Give the extent of all Plasmodium falciparum-infected red blood cells.
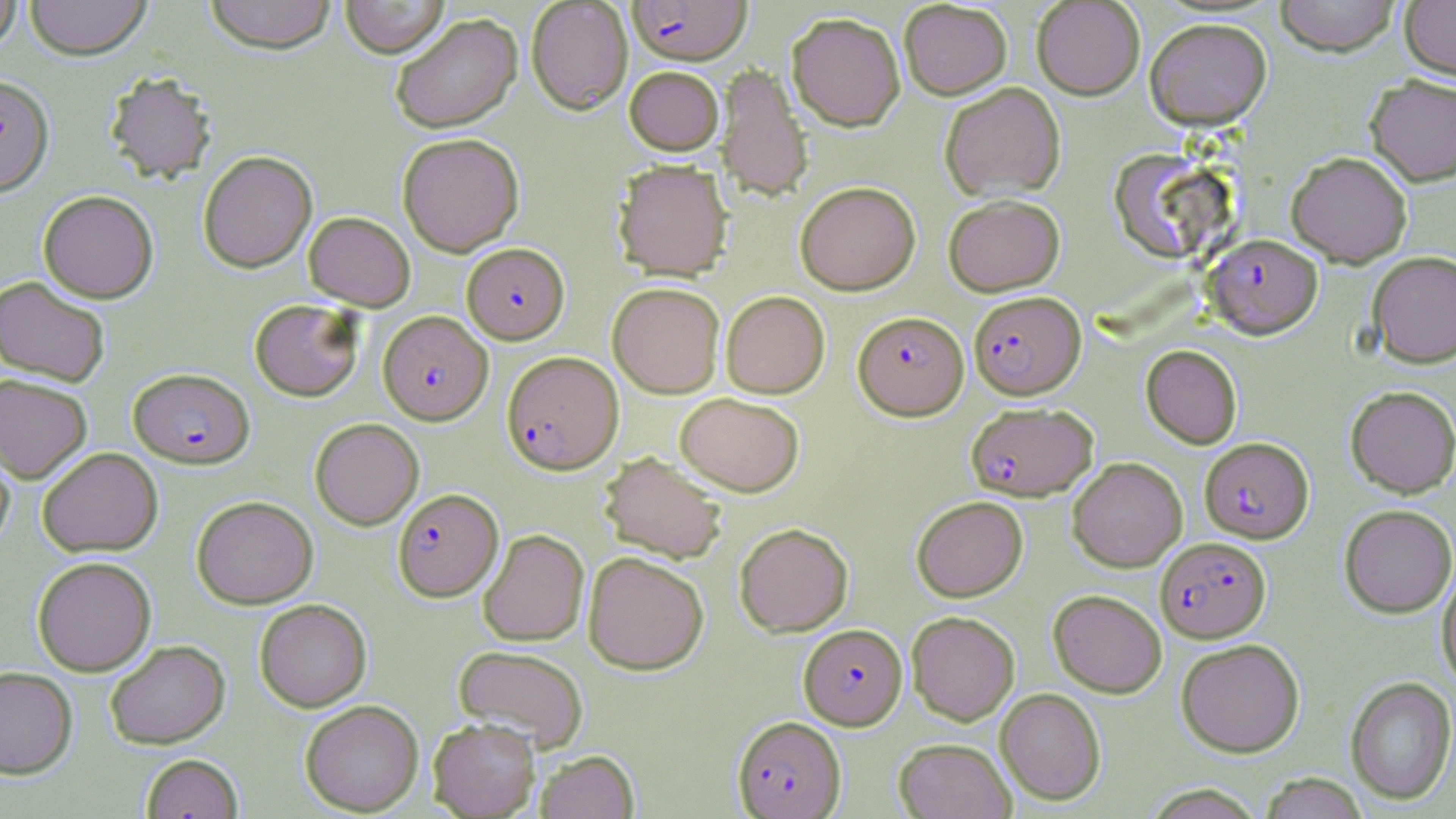

Approximate bounding boxes as [x1, y1, x2, y2] in pixels.
Plasmodium falciparum-infected red blood cells: [627, 0, 751, 66], [1205, 233, 1322, 339], [462, 243, 569, 344], [969, 291, 1085, 399], [378, 311, 492, 425], [854, 311, 968, 420], [501, 351, 623, 475], [128, 368, 255, 468], [966, 402, 1097, 501], [1199, 437, 1313, 543], [393, 488, 503, 602], [1156, 537, 1271, 642], [798, 623, 907, 730], [733, 716, 846, 818].

Summary:
  - Uninfected red blood cell locations: [0, 0, 22, 54], [24, 0, 151, 61], [205, 0, 337, 55], [340, 0, 450, 58], [899, 0, 1012, 100], [1032, 0, 1145, 100], [1274, 0, 1401, 56], [1400, 0, 1456, 80], [526, 1, 633, 114], [786, 12, 905, 130], [390, 13, 522, 134], [1144, 17, 1272, 130], [716, 63, 813, 202], [625, 66, 724, 156], [104, 71, 217, 185], [1366, 74, 1456, 186], [0, 75, 53, 196], [939, 82, 1065, 201], [397, 132, 524, 256], [1109, 149, 1227, 263], [198, 151, 317, 273], [1287, 151, 1412, 267], [613, 160, 733, 281], [795, 181, 920, 294], [38, 190, 159, 303], [943, 194, 1065, 296], [304, 212, 415, 311], [1368, 250, 1456, 367], [0, 275, 111, 387], [607, 282, 725, 398], [721, 291, 829, 398], [249, 299, 364, 401], [1141, 344, 1242, 448], [0, 373, 93, 483], [1345, 385, 1456, 498], [675, 392, 805, 497], [310, 418, 424, 530], [0, 436, 15, 554], [38, 447, 163, 557], [599, 452, 728, 565], [1067, 457, 1187, 571], [191, 495, 318, 609], [912, 496, 1028, 601], [1339, 504, 1456, 617], [734, 523, 853, 636], [478, 529, 589, 646], [583, 551, 709, 675], [32, 556, 156, 676], [1437, 565, 1456, 688], [1048, 589, 1167, 697], [255, 599, 372, 712], [906, 611, 1020, 725], [1176, 638, 1304, 757], [105, 640, 230, 749], [453, 644, 589, 752], [0, 666, 77, 779], [1345, 676, 1456, 806], [995, 687, 1106, 805], [300, 700, 423, 815], [428, 718, 540, 818], [894, 737, 1015, 818], [535, 750, 639, 819], [141, 753, 243, 818], [1258, 773, 1369, 819]
  - Slide-level diagnosis: Plasmodium falciparum
  - Modality: optical microscopy
  - Stain: May-Grünwald-Giemsa
  - Magnification: 1000x
  - Image size: 1456×819 pixels
  - Preparation: thin blood smear
  - Field of view: single